State the blood parasite species.
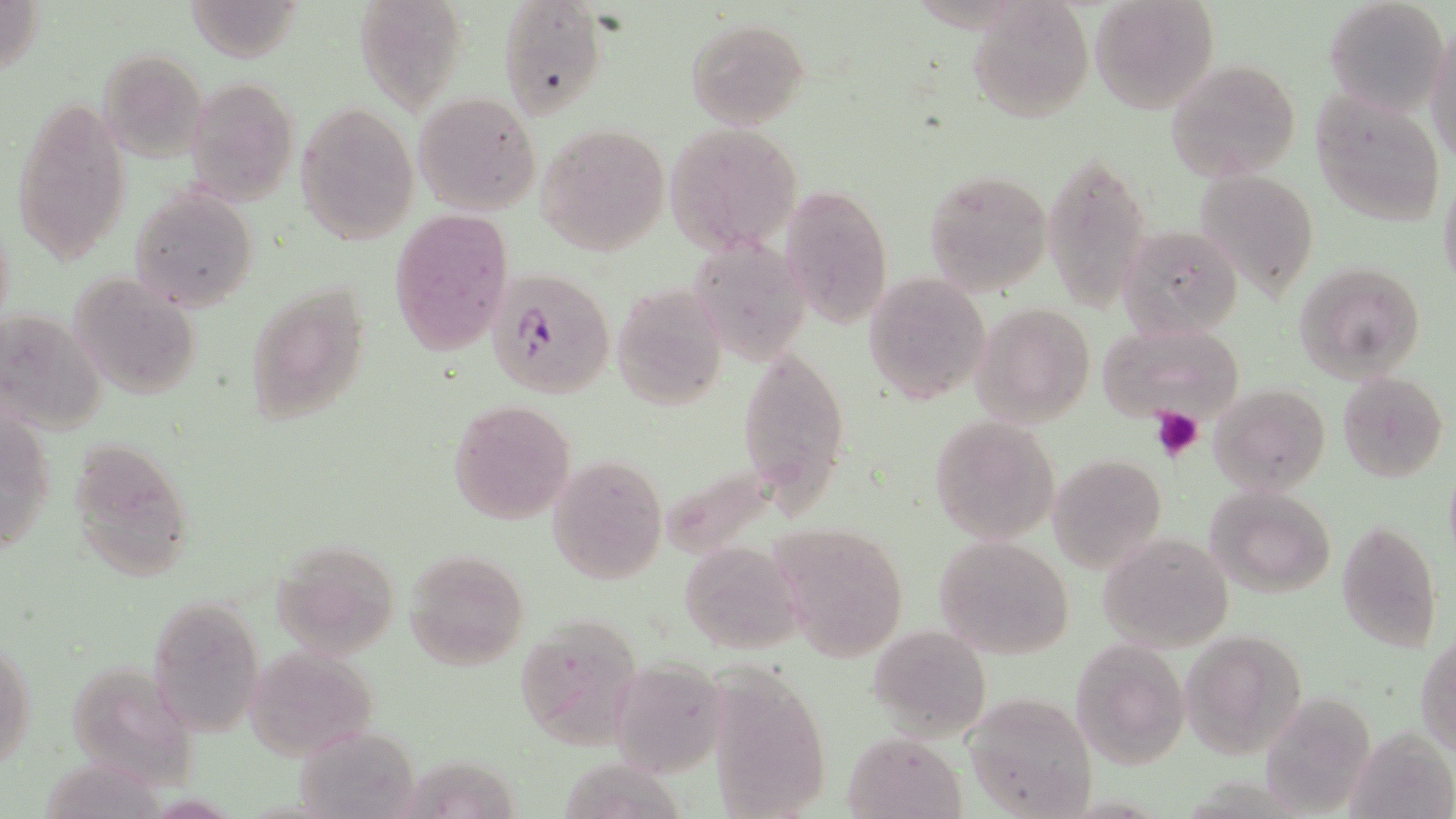
Plasmodium falciparum.

Approximate bounding boxes as named x1/y1/x2/y2 corners in pixels. Platelet locations: (x1=1151, y1=407, x2=1203, y2=462). Plasmodium falciparum-infected red blood cell locations: (x1=487, y1=268, x2=615, y2=399). Uninfected red blood cell locations: (x1=1, y1=0, x2=45, y2=78), (x1=352, y1=0, x2=469, y2=114), (x1=967, y1=0, x2=1093, y2=122), (x1=1089, y1=0, x2=1220, y2=114), (x1=1323, y1=0, x2=1450, y2=119), (x1=497, y1=1, x2=608, y2=116), (x1=686, y1=18, x2=809, y2=129), (x1=1425, y1=22, x2=1456, y2=168), (x1=96, y1=48, x2=208, y2=161), (x1=1164, y1=58, x2=1302, y2=183), (x1=184, y1=76, x2=299, y2=204), (x1=1308, y1=89, x2=1447, y2=226), (x1=413, y1=91, x2=542, y2=215), (x1=8, y1=95, x2=133, y2=266), (x1=296, y1=102, x2=418, y2=245), (x1=664, y1=123, x2=802, y2=255), (x1=535, y1=124, x2=670, y2=255), (x1=1043, y1=148, x2=1153, y2=313), (x1=923, y1=168, x2=1053, y2=297), (x1=1196, y1=169, x2=1321, y2=303), (x1=1438, y1=176, x2=1456, y2=296), (x1=780, y1=181, x2=893, y2=331), (x1=131, y1=187, x2=258, y2=312), (x1=389, y1=209, x2=514, y2=357), (x1=1119, y1=224, x2=1243, y2=341), (x1=690, y1=237, x2=812, y2=367), (x1=1296, y1=261, x2=1425, y2=382), (x1=68, y1=272, x2=201, y2=401), (x1=863, y1=272, x2=990, y2=402), (x1=246, y1=281, x2=371, y2=427), (x1=611, y1=281, x2=727, y2=410), (x1=972, y1=302, x2=1095, y2=427), (x1=4, y1=318, x2=107, y2=432), (x1=1096, y1=322, x2=1245, y2=428), (x1=739, y1=346, x2=849, y2=506), (x1=1336, y1=371, x2=1449, y2=482), (x1=1209, y1=382, x2=1331, y2=496), (x1=447, y1=399, x2=578, y2=524), (x1=928, y1=416, x2=1059, y2=544), (x1=1, y1=417, x2=55, y2=546), (x1=65, y1=436, x2=197, y2=583), (x1=547, y1=452, x2=669, y2=586), (x1=653, y1=453, x2=786, y2=562), (x1=1048, y1=454, x2=1166, y2=573), (x1=1442, y1=463, x2=1456, y2=568), (x1=1204, y1=485, x2=1338, y2=598), (x1=1336, y1=520, x2=1444, y2=652), (x1=771, y1=523, x2=907, y2=659), (x1=1098, y1=531, x2=1235, y2=652), (x1=934, y1=535, x2=1075, y2=659), (x1=270, y1=540, x2=402, y2=659), (x1=678, y1=542, x2=805, y2=657), (x1=402, y1=549, x2=529, y2=670), (x1=145, y1=597, x2=264, y2=737), (x1=511, y1=612, x2=644, y2=751), (x1=867, y1=625, x2=992, y2=743), (x1=1180, y1=629, x2=1308, y2=758), (x1=1417, y1=635, x2=1456, y2=756), (x1=1071, y1=640, x2=1191, y2=770), (x1=1, y1=641, x2=34, y2=773), (x1=246, y1=646, x2=378, y2=758), (x1=621, y1=651, x2=733, y2=776), (x1=700, y1=656, x2=834, y2=818), (x1=59, y1=659, x2=209, y2=776), (x1=1258, y1=689, x2=1379, y2=815), (x1=963, y1=691, x2=1100, y2=816), (x1=292, y1=724, x2=424, y2=817), (x1=1344, y1=728, x2=1456, y2=819), (x1=844, y1=731, x2=965, y2=818), (x1=562, y1=748, x2=685, y2=814), (x1=405, y1=757, x2=523, y2=816). Captured at 1000x magnification. May-Grünwald-Giemsa-stained preparation. One field of a larger specimen. Thin blood film. Image is 1456×819 pixels. Optical microscopy.